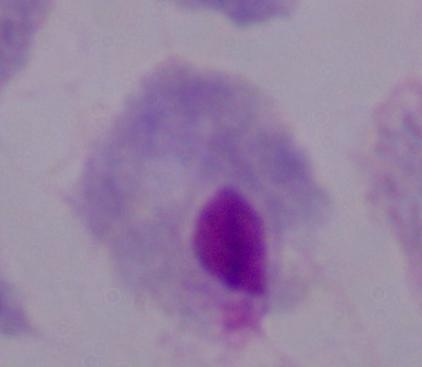
Summary:
  - Identification: trichomonad
  - Magnification: 1000x
  - Modality: photomicrograph